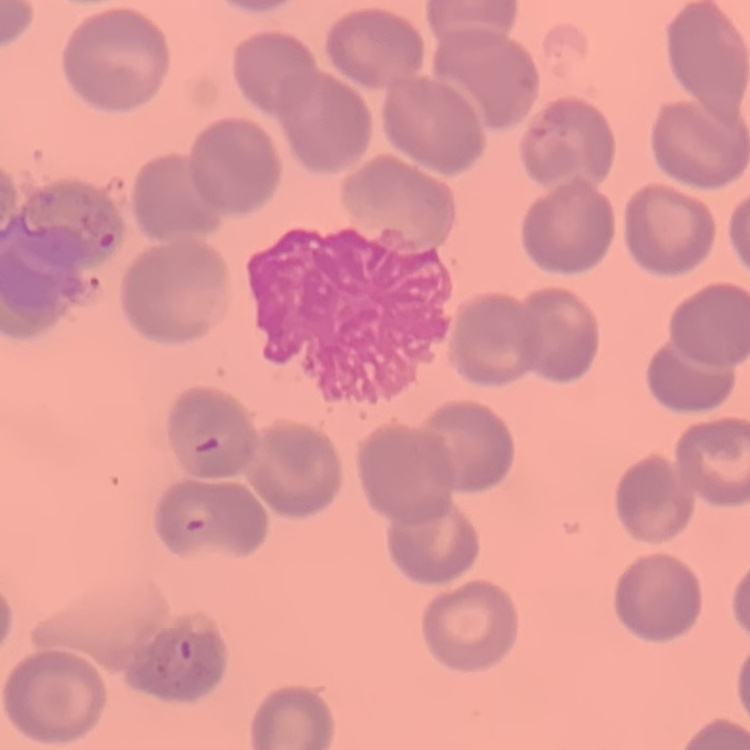
Summary:
  - Erythrocyte morphology: no rouleaux formation
  - Preparation: thin blood film
  - Image type: one tile cut from a larger photomicrograph
  - Stain: Field's or Giemsa